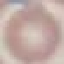

Summary:
  - Result: no malaria parasites detected
  - Preparation: thin smear
  - Stain: Giemsa
  - Capture: smartphone through the microscope eyepiece
  - Image type: automatically extracted cell patch, resized to 64 × 64 pixels